Classify this cell by malaria status.
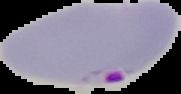
Parasitized.

Summary:
  - Preparation: thin blood smear
  - Image size: 181×94 pixels
  - Image type: segmented cell region on a black background